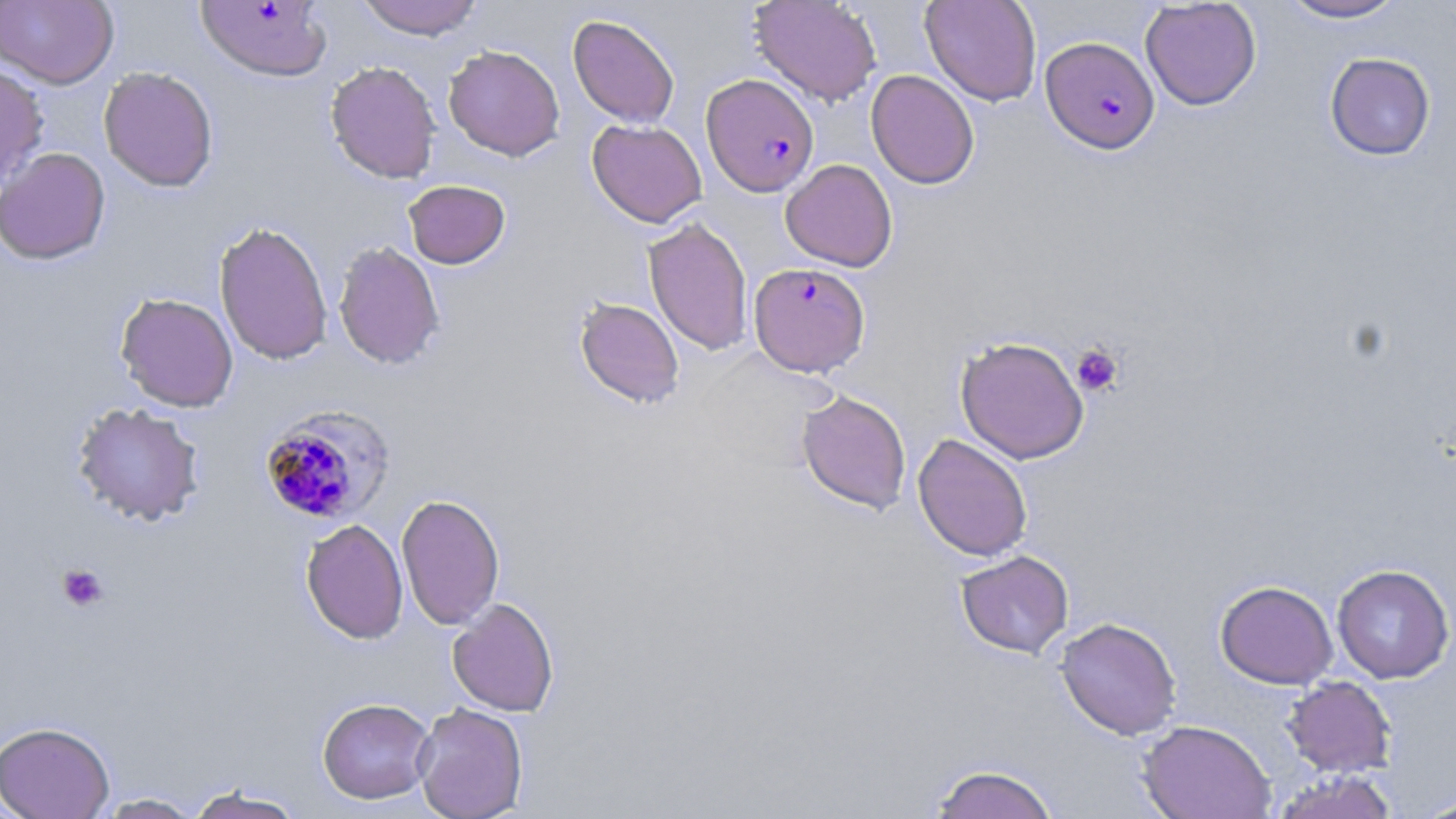
Approximate bounding boxes as [x1, y1, x2, y2] in pixels. Uninfected red blood cell locations: [0, 0, 119, 89], [355, 0, 484, 40], [749, 0, 882, 107], [920, 0, 1042, 107], [1278, 0, 1409, 23], [1140, 1, 1261, 111], [568, 14, 680, 127], [443, 45, 564, 161], [1324, 52, 1436, 160], [325, 60, 441, 184], [0, 62, 49, 190], [98, 66, 219, 192], [865, 70, 979, 189], [587, 119, 707, 227], [0, 147, 111, 264], [780, 159, 898, 271], [403, 179, 510, 269], [643, 217, 754, 356], [214, 221, 333, 366], [333, 241, 445, 370], [115, 293, 239, 412], [574, 296, 685, 409], [955, 335, 1089, 464], [796, 389, 911, 514], [72, 402, 205, 526], [912, 433, 1033, 562], [396, 493, 505, 630], [301, 518, 408, 644], [956, 551, 1074, 658], [1332, 563, 1454, 684], [1216, 580, 1338, 689], [447, 597, 559, 716], [1055, 617, 1181, 740], [1282, 676, 1396, 777], [317, 697, 435, 804], [413, 702, 528, 819], [1137, 718, 1276, 819], [0, 720, 115, 819], [927, 763, 1061, 819], [1271, 770, 1399, 819], [183, 784, 307, 819], [95, 793, 203, 818], [1415, 795, 1456, 818]. Plasmodium falciparum-infected red blood cell locations: [195, 1, 332, 82], [1040, 36, 1160, 154], [701, 73, 819, 197], [749, 262, 870, 376], [258, 405, 396, 525]. Platelet locations: [1071, 344, 1123, 396], [56, 563, 109, 612]. Slide-level diagnosis: Plasmodium falciparum. 1000x magnification. Light microscopy. May-Grünwald-Giemsa stain. Thin blood smear. Image is 1456×819 pixels. One field of a larger specimen.